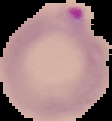
Malaria status: parasitized. From a thin blood film. Image is 112×121 pixels. Cell region segmented out of the field of view; the surrounding area is masked to black.